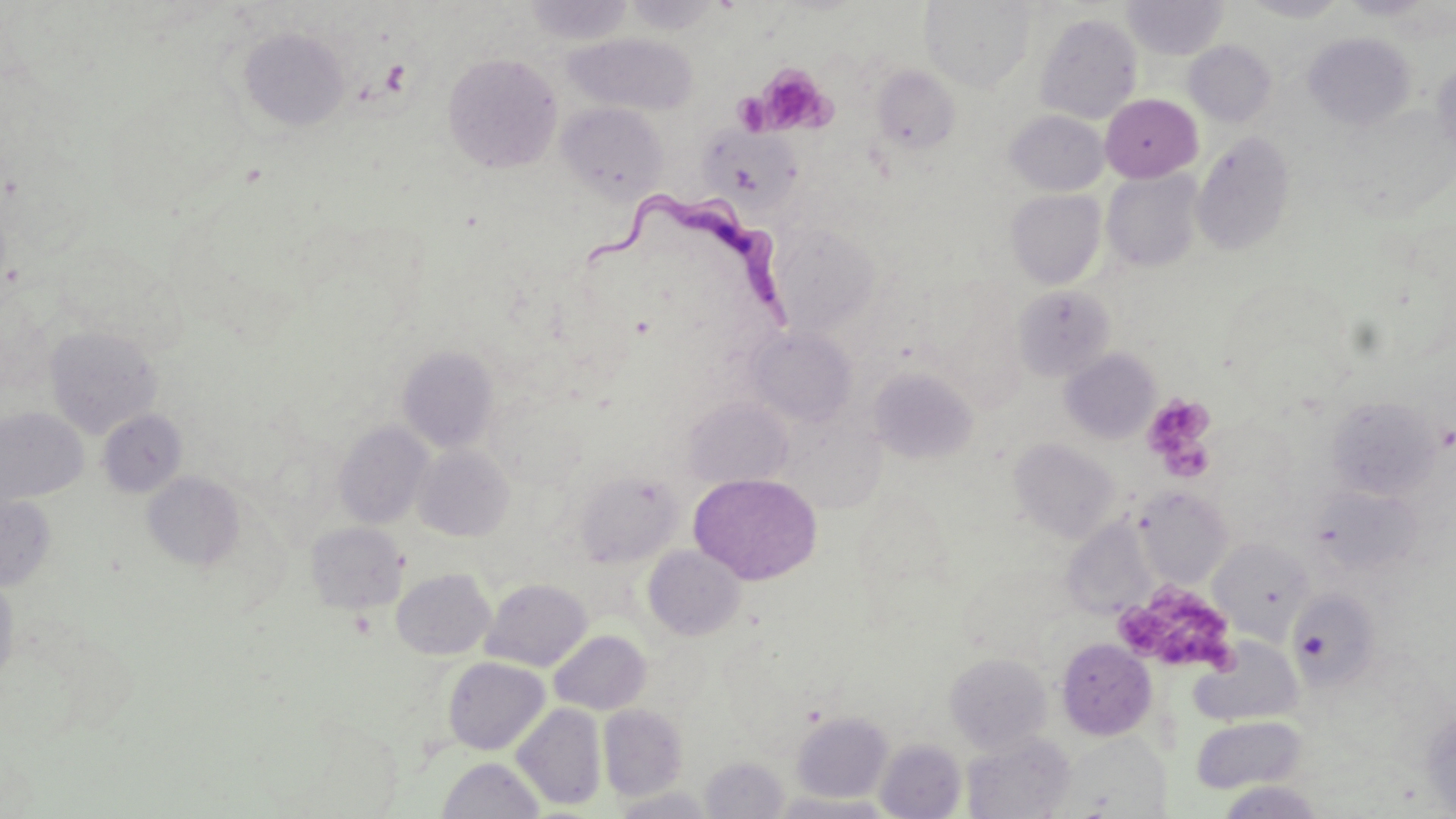
Approximate bounding boxes as named x1/y1/x2/y2 corners in pixels. Platelet locations: (x1=756, y1=62, x2=837, y2=135), (x1=1143, y1=394, x2=1215, y2=469), (x1=1121, y1=589, x2=1241, y2=676). Uninfected red blood cell locations: (x1=522, y1=0, x2=635, y2=46), (x1=622, y1=0, x2=724, y2=34), (x1=921, y1=0, x2=1035, y2=92), (x1=1122, y1=0, x2=1229, y2=59), (x1=1239, y1=0, x2=1352, y2=22), (x1=1035, y1=12, x2=1143, y2=124), (x1=237, y1=27, x2=350, y2=132), (x1=1303, y1=32, x2=1415, y2=131), (x1=567, y1=33, x2=699, y2=115), (x1=1183, y1=40, x2=1277, y2=127), (x1=442, y1=52, x2=562, y2=174), (x1=1431, y1=59, x2=1456, y2=159), (x1=871, y1=65, x2=961, y2=156), (x1=1100, y1=94, x2=1202, y2=182), (x1=556, y1=102, x2=668, y2=202), (x1=1338, y1=105, x2=1454, y2=220), (x1=1006, y1=110, x2=1108, y2=195), (x1=701, y1=124, x2=803, y2=215), (x1=1192, y1=130, x2=1295, y2=256), (x1=1101, y1=170, x2=1203, y2=272), (x1=1006, y1=189, x2=1106, y2=288), (x1=768, y1=223, x2=881, y2=336), (x1=1013, y1=285, x2=1116, y2=381), (x1=45, y1=325, x2=162, y2=438), (x1=750, y1=327, x2=856, y2=427), (x1=398, y1=346, x2=499, y2=453), (x1=1060, y1=348, x2=1160, y2=444), (x1=868, y1=366, x2=979, y2=464), (x1=682, y1=396, x2=792, y2=489), (x1=1326, y1=396, x2=1442, y2=500), (x1=0, y1=406, x2=88, y2=506), (x1=97, y1=409, x2=187, y2=498), (x1=334, y1=421, x2=434, y2=529), (x1=1008, y1=437, x2=1120, y2=543), (x1=414, y1=445, x2=514, y2=541), (x1=574, y1=469, x2=683, y2=567), (x1=142, y1=471, x2=245, y2=572), (x1=689, y1=473, x2=823, y2=585), (x1=1310, y1=485, x2=1422, y2=576), (x1=1135, y1=487, x2=1233, y2=587), (x1=853, y1=488, x2=954, y2=607), (x1=0, y1=491, x2=57, y2=591), (x1=1070, y1=506, x2=1158, y2=616), (x1=306, y1=521, x2=407, y2=613), (x1=1209, y1=538, x2=1313, y2=641), (x1=643, y1=545, x2=746, y2=641), (x1=392, y1=568, x2=495, y2=660), (x1=0, y1=571, x2=20, y2=688), (x1=481, y1=577, x2=591, y2=671), (x1=1289, y1=589, x2=1381, y2=688), (x1=549, y1=630, x2=651, y2=714), (x1=1191, y1=637, x2=1302, y2=726), (x1=1056, y1=638, x2=1156, y2=740), (x1=944, y1=653, x2=1052, y2=753), (x1=443, y1=657, x2=549, y2=755), (x1=512, y1=703, x2=606, y2=811), (x1=599, y1=704, x2=688, y2=800), (x1=1421, y1=705, x2=1456, y2=817), (x1=791, y1=711, x2=893, y2=803), (x1=1191, y1=716, x2=1306, y2=794), (x1=962, y1=732, x2=1076, y2=819), (x1=875, y1=739, x2=965, y2=818), (x1=437, y1=756, x2=545, y2=819), (x1=701, y1=756, x2=790, y2=819), (x1=1217, y1=781, x2=1325, y2=818), (x1=610, y1=784, x2=717, y2=818), (x1=773, y1=792, x2=896, y2=819). Trypanosoma brucei locations: (x1=580, y1=190, x2=800, y2=338). Slide-level diagnosis: Trypanosoma brucei. Light microscopy. Image is 1456×819 pixels. Thin blood film. One field of a larger specimen. May-Grünwald-Giemsa stain. Captured at 1000x magnification.